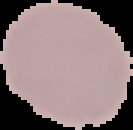

Summary:
  - Image type: segmented cell region on a black background
  - Malaria status: uninfected
  - Image size: 133×130 pixels
  - Preparation: thin blood film